Give the position of every Plasmodium parasite visible.
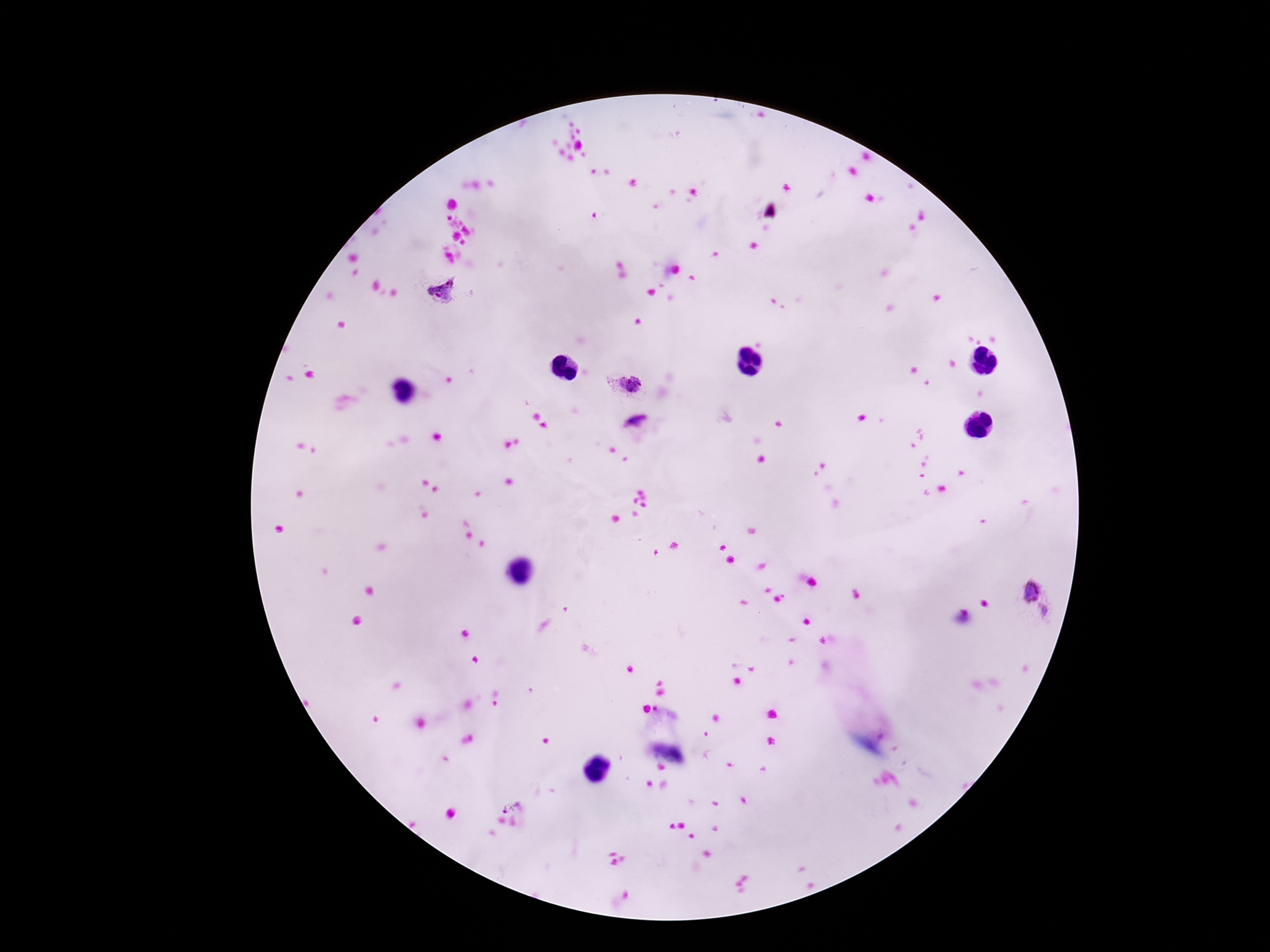
Approximate centers as (x, y) in pixels.
Plasmodium parasites: (439, 290), (627, 383), (1029, 591), (1044, 613), (510, 803).

Summary:
  - Patient malaria status: infected
  - Magnification: 100x
  - Capture: smartphone camera through the microscope eyepiece
  - Preparation: thick blood film
  - Image size: 1270×952 pixels
  - Stain: Giemsa
  - Field of view: single